Assess this cell for malaria.
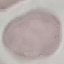
It is uninfected.

Giemsa-stained preparation. Photographed with a smartphone camera at the microscope eyepiece. Cell patch, automatically extracted from a larger field of view and resized to 64 × 64 pixels. Thin blood smear.